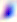
Summary:
  - Magnification: 400x
  - Identification: Toxoplasma gondii
  - Modality: micrograph